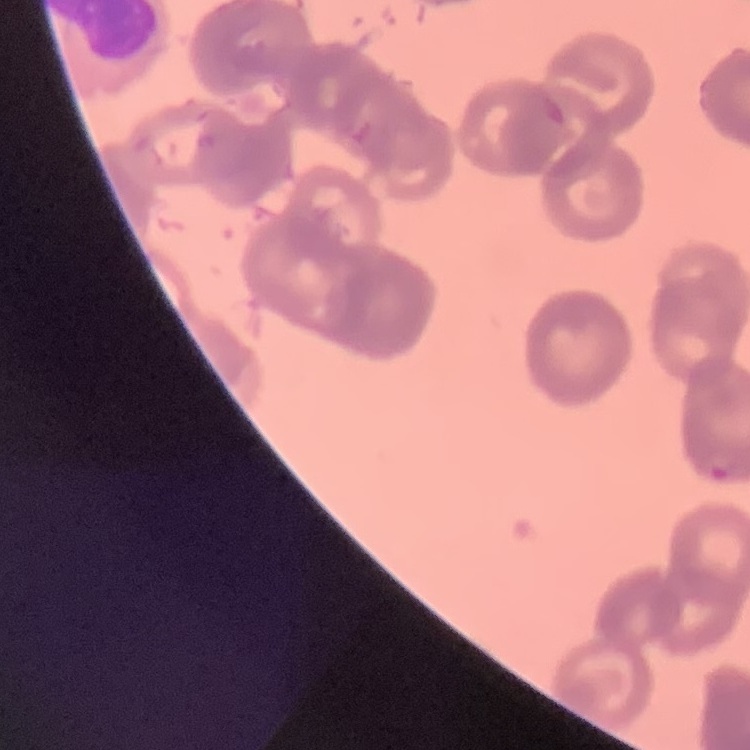
Summary:
  - Erythrocyte morphology: rouleaux formation
  - Preparation: thin blood smear
  - Stain: Field's or Giemsa
  - Image type: square crop of a larger photomicrograph